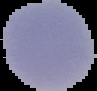

Summary:
  - Result: no malaria parasites seen
  - Image type: segmented cell region with the area outside set to black
  - Preparation: thin blood smear
  - Image size: 97×91 pixels